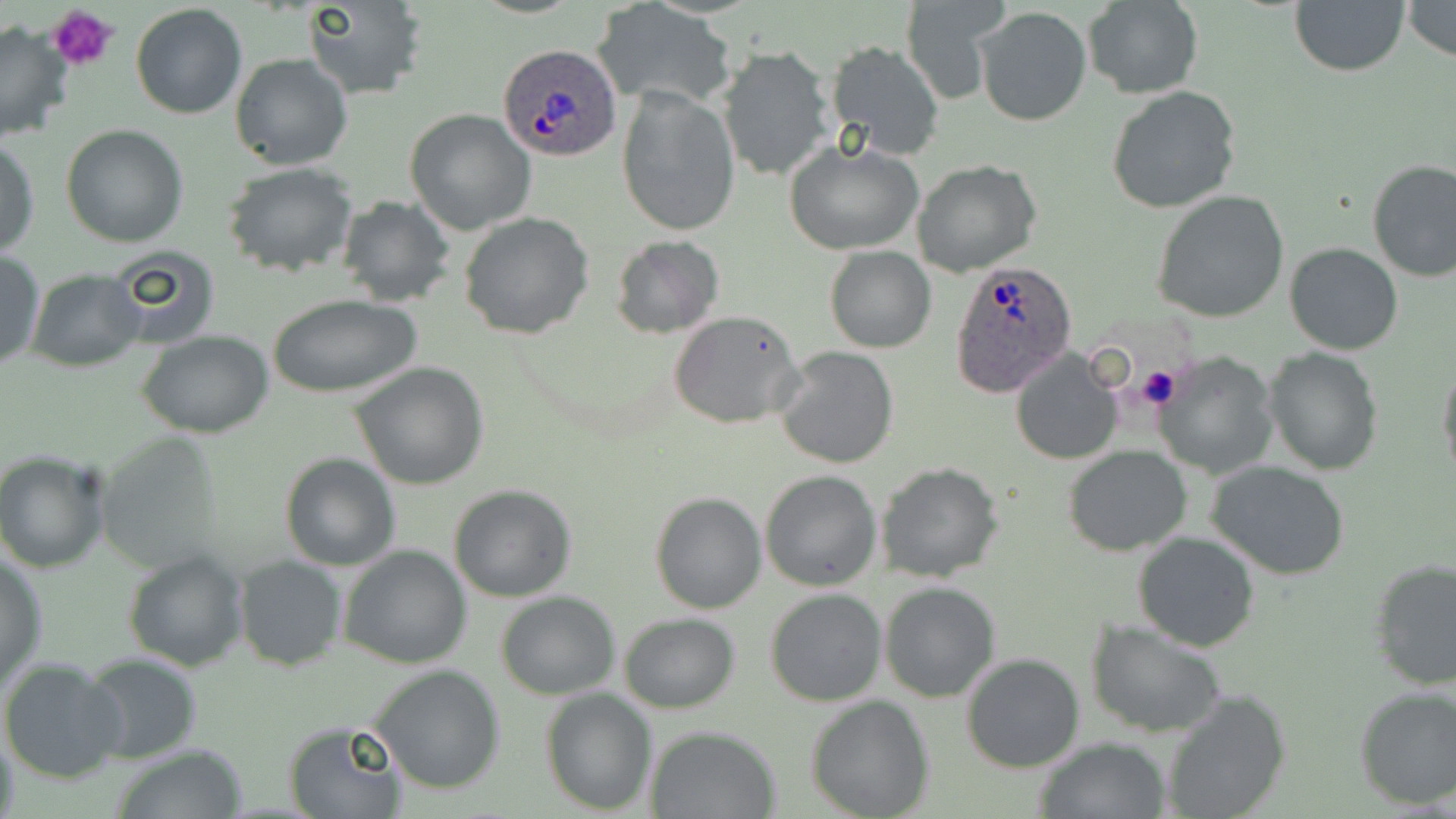
{
  "slide_level_diagnosis": "Plasmodium ovale",
  "preparation": "thin blood smear",
  "uninfected_red_blood_cell_locations": "approximate bounding boxes as [x1, y1, x2, y2] in pixels: [300, 0, 429, 99], [900, 0, 1008, 104], [1290, 0, 1409, 75], [1400, 0, 1456, 62], [1082, 1, 1202, 98], [130, 3, 248, 118], [594, 4, 735, 111], [972, 7, 1093, 127], [0, 18, 74, 143], [822, 39, 945, 163], [716, 47, 834, 182], [229, 54, 355, 172], [1105, 85, 1243, 214], [616, 87, 740, 237], [404, 109, 537, 235], [60, 124, 189, 248], [1, 138, 40, 258], [782, 140, 924, 254], [1366, 158, 1456, 282], [911, 161, 1041, 278], [221, 163, 360, 278], [1152, 189, 1292, 323], [335, 194, 455, 308], [459, 211, 596, 339], [609, 235, 724, 339], [1284, 242, 1403, 355], [824, 247, 936, 353], [106, 248, 223, 351], [0, 252, 45, 371], [24, 270, 146, 371], [271, 293, 422, 399], [669, 309, 807, 429], [136, 330, 275, 438], [774, 345, 900, 468], [1263, 347, 1384, 476], [1010, 349, 1123, 464], [1153, 350, 1280, 479], [1437, 360, 1456, 484], [350, 361, 490, 490], [94, 431, 229, 570], [1062, 445, 1193, 557], [1, 451, 113, 572], [281, 452, 400, 572], [1206, 461, 1354, 581], [877, 462, 1004, 583], [760, 470, 883, 591], [449, 485, 577, 602], [649, 492, 766, 614], [1132, 531, 1260, 652], [337, 544, 473, 669], [1, 550, 48, 694], [122, 550, 248, 672], [234, 555, 346, 671], [1367, 559, 1456, 689], [880, 581, 1000, 700], [765, 588, 888, 707], [495, 591, 620, 698], [617, 613, 740, 713], [1086, 618, 1228, 739], [81, 653, 202, 765], [961, 653, 1086, 773], [0, 659, 128, 785], [368, 666, 508, 796], [1353, 685, 1456, 809], [539, 687, 658, 814], [1160, 688, 1291, 819], [805, 695, 934, 818], [283, 722, 404, 818], [645, 726, 780, 818], [1, 728, 20, 819], [1033, 736, 1172, 818], [109, 743, 250, 819]",
  "plasmodium_ovale_infected_red_blood_cell_locations": "approximate bounding boxes as [x1, y1, x2, y2] in pixels: [496, 45, 622, 161], [947, 259, 1076, 397]",
  "magnification": "1000x",
  "modality": "light microscopy",
  "stain": "May-Grünwald-Giemsa",
  "platelet_locations": "approximate bounding boxes as [x1, y1, x2, y2] in pixels: [47, 5, 120, 75], [1131, 364, 1182, 412]",
  "image_size": "1456×819 pixels",
  "field_of_view": "one of a larger specimen"
}